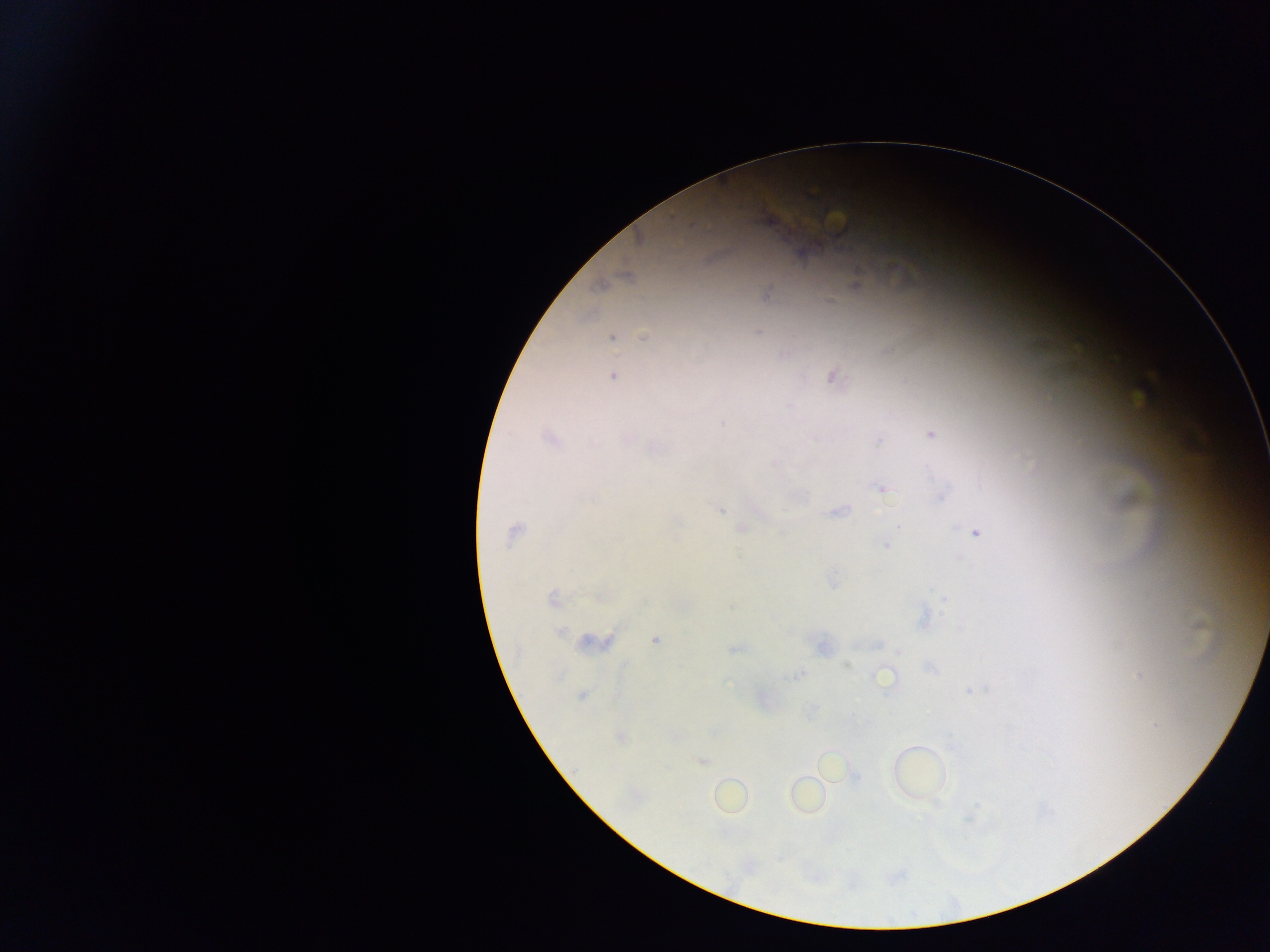
Approximate centers as x y in pixels.
Summary:
  - Malaria parasite locations: 625 278; 601 286; 855 286; 765 294; 829 302; 757 332; 643 337; 611 338; 614 376; 832 376; 723 422; 931 435; 628 438; 549 439; 878 441; 594 444; 656 448; 775 464; 882 489; 939 498; 720 509; 837 512; 676 518; 900 526; 741 528; 975 532; 514 534; 886 544; 959 557; 833 580; 599 596; 553 598; 944 598; 924 618; 1199 626; 561 632; 655 639; 593 643; 878 644; 821 646; 734 650; 899 651; 846 666; 929 668; 798 675; 1139 675; 885 677; 970 691; 582 696; 621 738; 702 762; 805 796
  - Preparation: thick blood smear
  - Image size: 1270×952 pixels
  - Country: Ghana
  - Field of view: single
  - Capture: mobile-phone photograph through a microscope